Assess the morphology of the red blood cells.
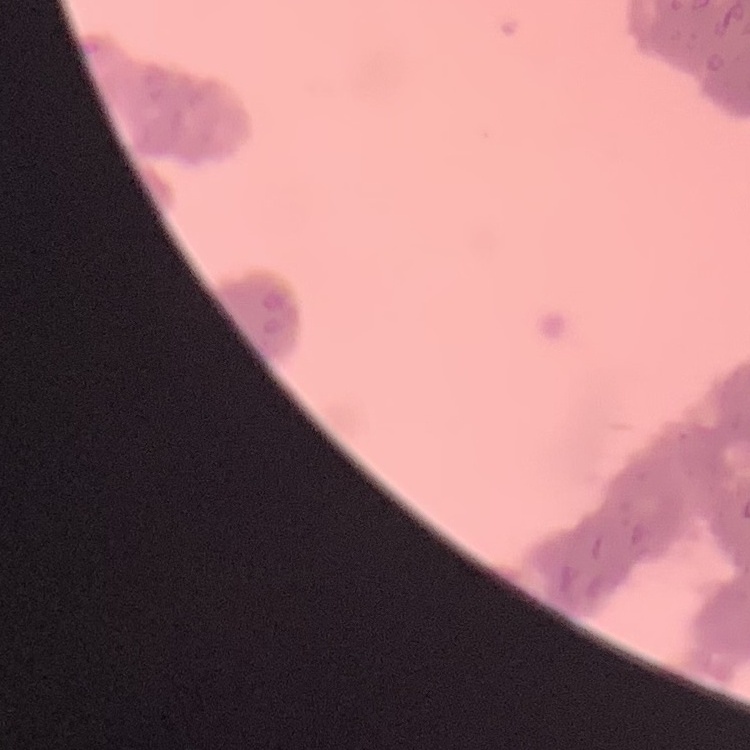

They show rouleaux formation.

Square crop of a larger photomicrograph. Thin blood film. Field's or Giemsa stain.